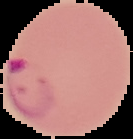

Summary:
  - Preparation: thin blood smear
  - Result: malaria parasites identified
  - Image size: 133×139 pixels
  - Image type: segmented cell region with the area outside set to black